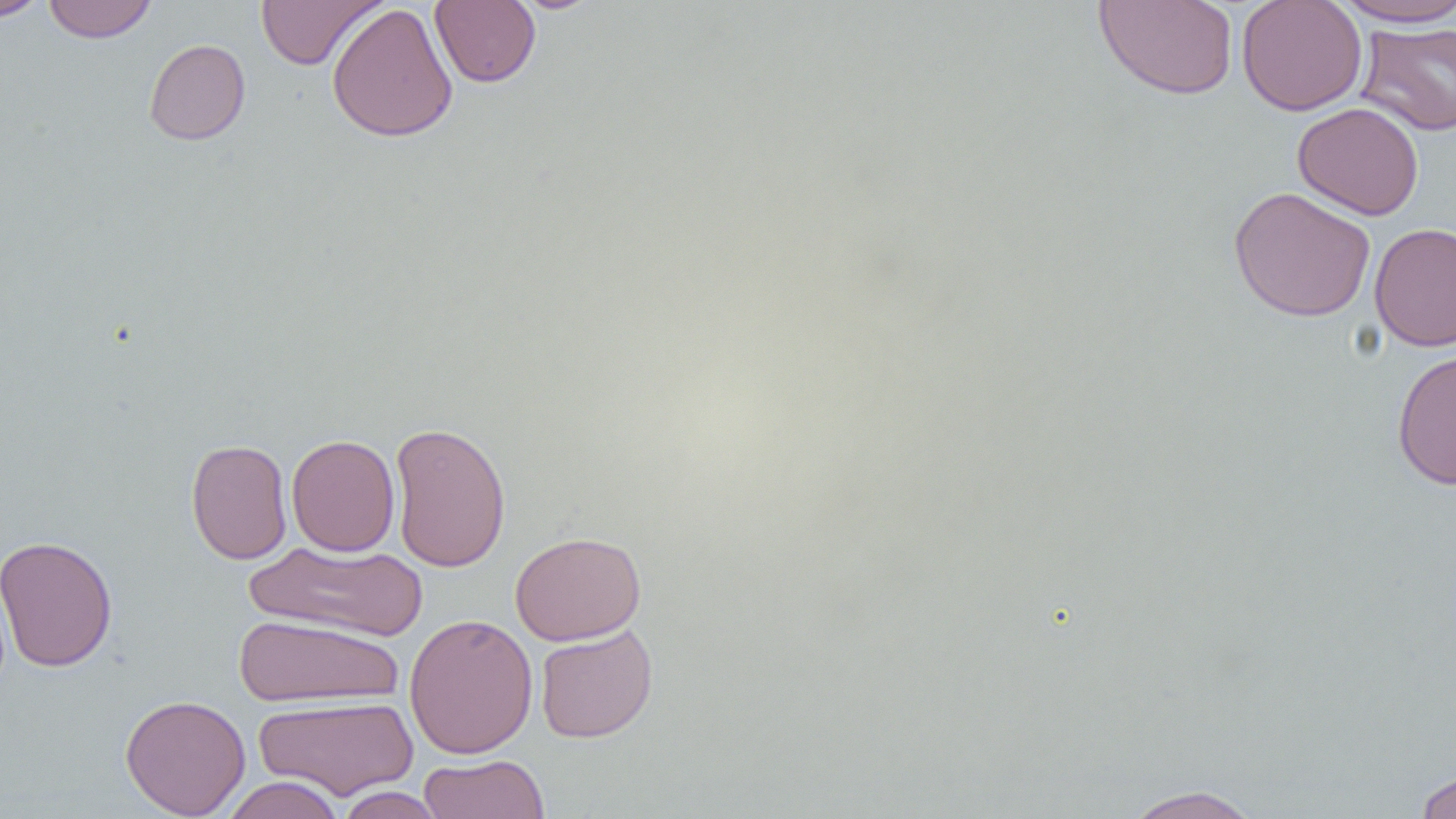

Approximate bounding boxes as [x1, y1, x2, y2] in pixels. Uninfected red blood cell locations: [1, 0, 51, 22], [42, 0, 158, 43], [256, 0, 385, 70], [429, 0, 541, 88], [510, 0, 604, 15], [1094, 0, 1239, 100], [1236, 0, 1367, 116], [1330, 0, 1455, 28], [326, 2, 458, 143], [1355, 21, 1456, 136], [143, 38, 250, 145], [1292, 102, 1424, 221], [1228, 186, 1376, 323], [1369, 221, 1456, 352], [1391, 348, 1456, 489], [389, 420, 511, 573], [286, 433, 400, 556], [185, 438, 292, 564], [510, 531, 646, 645], [0, 534, 118, 673], [242, 540, 429, 643], [404, 612, 538, 759], [233, 614, 405, 708], [535, 624, 658, 743], [120, 694, 251, 818], [253, 696, 418, 800], [418, 753, 550, 819], [1412, 769, 1456, 819], [220, 775, 346, 819], [1120, 785, 1266, 819], [334, 786, 446, 819]. Slide-level diagnosis: no evidence of blood parasites. Thin blood smear. Single field of view. 1000x magnification. Image is 1456×819 pixels. Light microscopy.